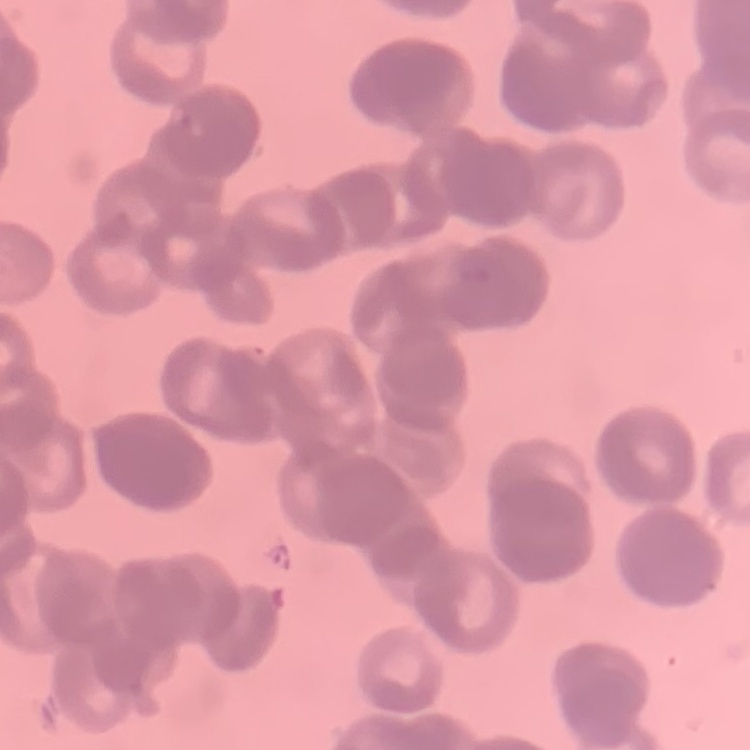

Summary:
  - Red blood cell morphology: rouleaux formation
  - Preparation: thin blood film
  - Stain: Field's or Giemsa
  - Image type: square crop of a larger photomicrograph